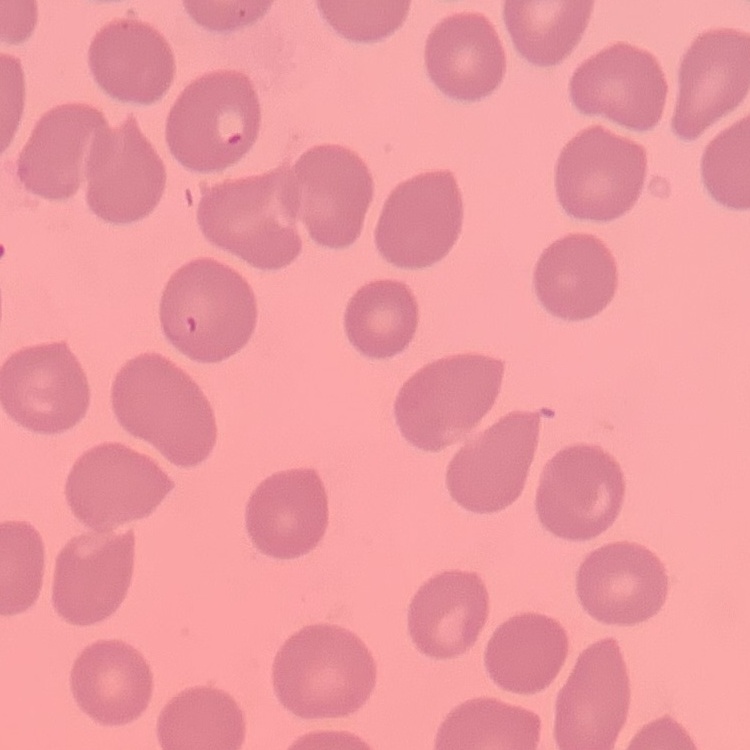

{
  "erythrocyte_morphology": "no rouleaux formation",
  "image_type": "one tile cut from a larger photomicrograph",
  "stain": "Field's or Giemsa",
  "preparation": "thin blood smear"
}